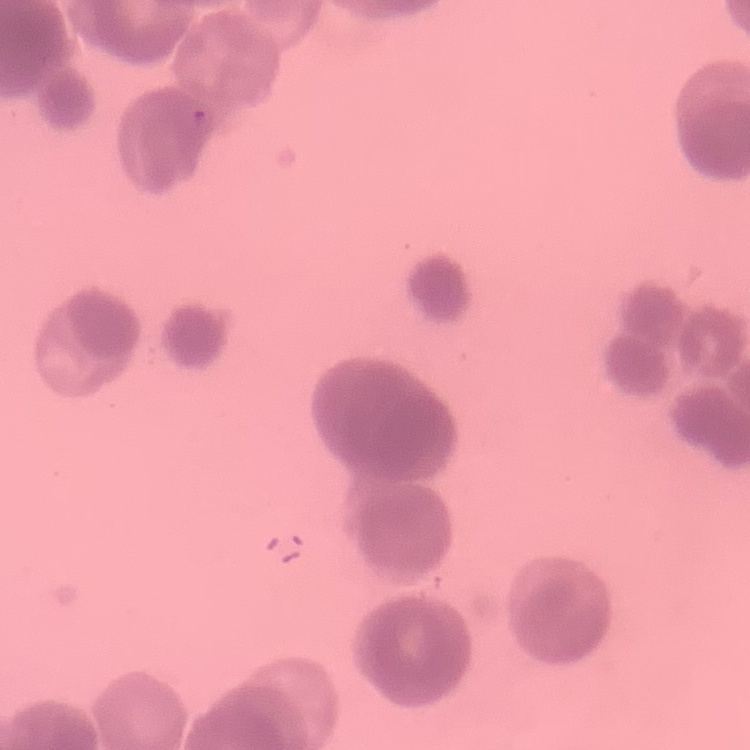

Summary:
  - Erythrocyte morphology: rouleaux formation
  - Image type: square crop of a larger photomicrograph
  - Preparation: thin blood smear
  - Stain: Field's or Giemsa